Report the malaria status of this cell.
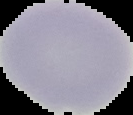
It is uninfected.

image size = 133×115 pixels
preparation = thin blood smear
image type = segmented cell region with the area outside set to black